Identify the blood parasite species.
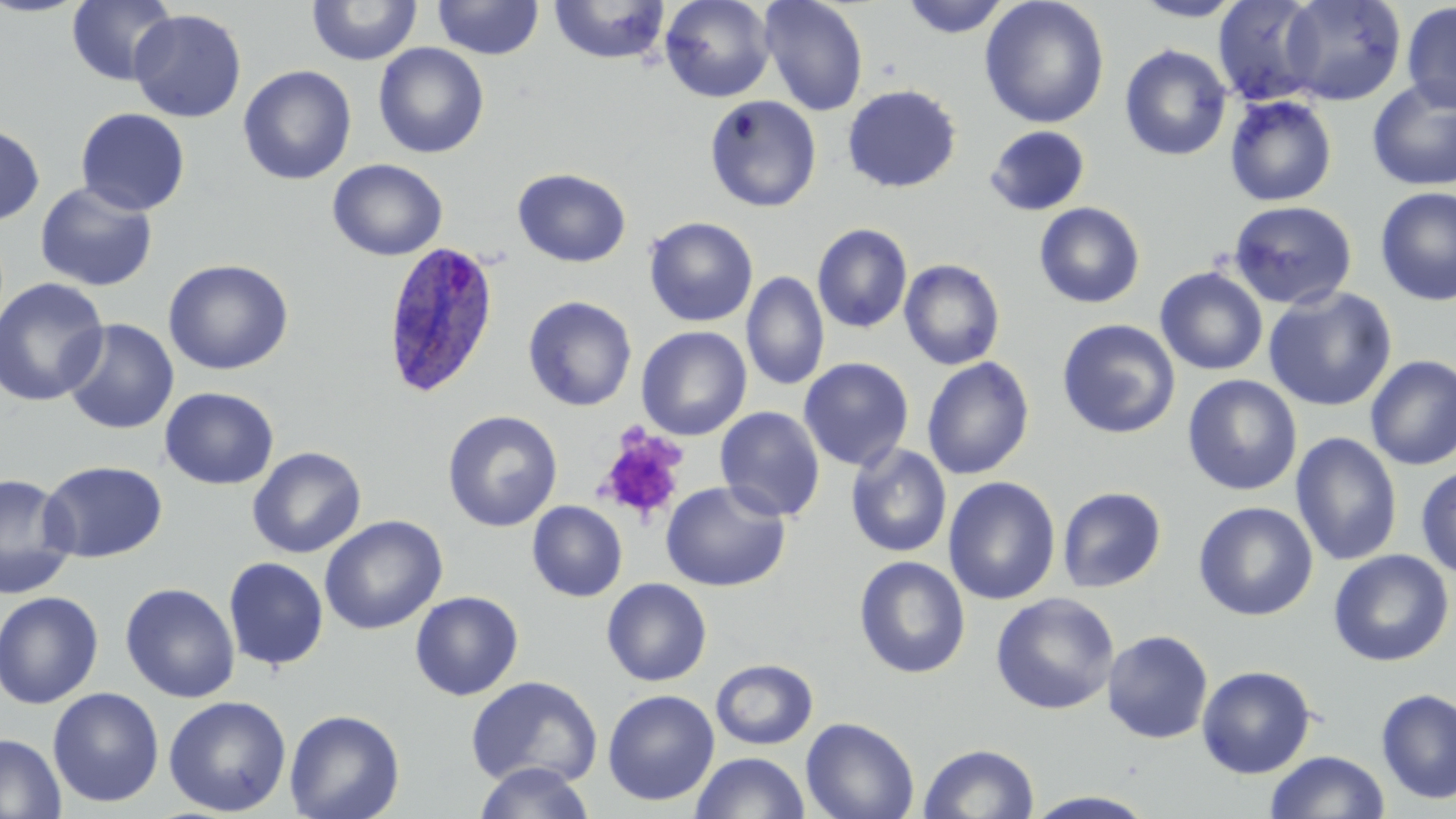

Plasmodium ovale.

platelet locations = approximate bounding boxes as (x1, y1, x2, y2) in pixels: (596, 428, 688, 524)
stain = May-Grünwald-Giemsa
image size = 1456×819 pixels
modality = light microscopy
Plasmodium ovale-infected red blood cell locations = approximate bounding boxes as (x1, y1, x2, y2) in pixels: (380, 240, 502, 399)
field of view = one of a larger specimen
magnification = 1000x
preparation = thin blood smear
uninfected red blood cell locations = approximate bounding boxes as (x1, y1, x2, y2) in pixels: (0, 0, 90, 17), (67, 0, 178, 86), (432, 0, 544, 61), (549, 0, 671, 65), (660, 0, 775, 102), (758, 0, 869, 116), (900, 0, 1013, 38), (979, 0, 1110, 129), (1131, 0, 1247, 22), (1213, 0, 1326, 106), (1279, 0, 1406, 106), (307, 1, 422, 66), (1401, 1, 1456, 113), (129, 9, 247, 122), (373, 43, 489, 158), (1119, 44, 1232, 161), (238, 65, 357, 185), (1366, 79, 1456, 192), (842, 84, 962, 193), (1224, 95, 1338, 207), (704, 96, 822, 212), (75, 108, 190, 216), (0, 121, 45, 225), (984, 125, 1090, 217), (327, 158, 447, 260), (513, 168, 632, 267), (35, 182, 158, 292), (1375, 187, 1456, 306), (1227, 200, 1357, 310), (1034, 202, 1145, 309), (644, 216, 758, 327), (812, 223, 912, 333), (163, 258, 294, 376), (899, 258, 1005, 370), (1155, 267, 1269, 376), (741, 271, 829, 391), (0, 277, 109, 407), (1263, 286, 1398, 412), (522, 295, 637, 411), (60, 318, 179, 435), (1057, 318, 1180, 439), (637, 326, 752, 440), (1365, 355, 1456, 470), (798, 357, 914, 471), (921, 357, 1035, 480), (1182, 374, 1303, 496), (159, 386, 280, 490), (715, 406, 825, 522), (443, 410, 563, 532), (1290, 432, 1403, 566), (845, 444, 952, 557), (247, 446, 366, 558), (39, 460, 168, 564), (1415, 465, 1456, 579), (0, 472, 78, 600), (943, 476, 1061, 605), (660, 480, 790, 592), (1057, 486, 1167, 593), (527, 500, 627, 602), (1193, 501, 1318, 621), (320, 514, 448, 635), (1328, 550, 1454, 667), (854, 555, 971, 679), (223, 557, 329, 671), (602, 578, 712, 687), (120, 582, 240, 703), (0, 591, 104, 709), (410, 591, 524, 701), (990, 592, 1120, 715), (1102, 629, 1214, 744), (710, 659, 818, 750), (1196, 665, 1317, 779), (465, 675, 603, 789), (47, 687, 164, 808), (1375, 687, 1456, 805), (603, 689, 720, 806), (163, 695, 291, 817), (284, 709, 405, 819), (800, 716, 920, 819), (0, 732, 66, 819), (919, 742, 1040, 819), (1266, 750, 1390, 818), (691, 751, 810, 818), (472, 762, 597, 819), (1022, 790, 1160, 818)